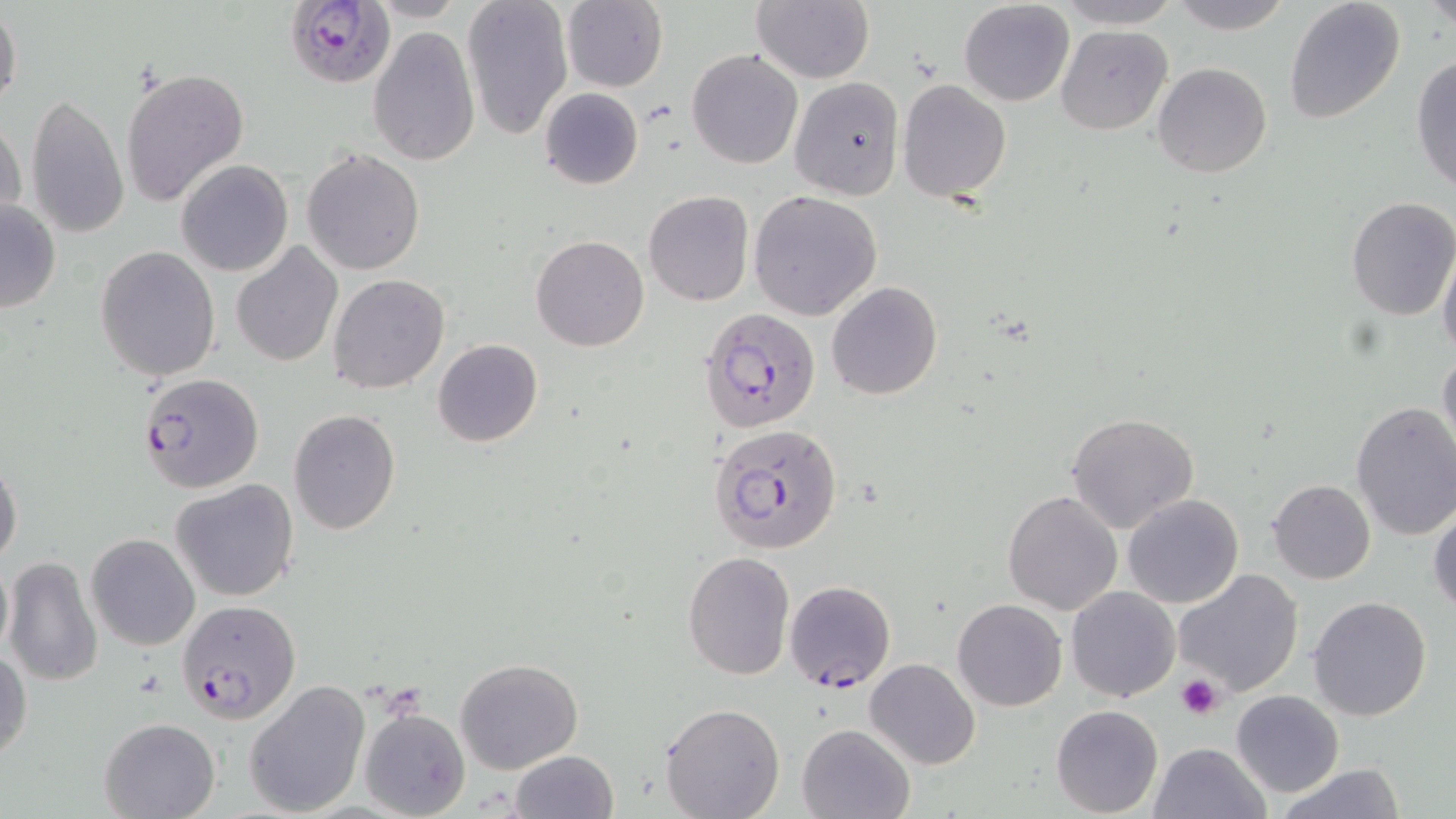
Approximate bounding boxes as (x1, y1, x2, y2) in pixels. Uninfected red blood cell locations: (462, 0, 573, 141), (561, 0, 668, 92), (751, 0, 874, 84), (1165, 0, 1294, 33), (958, 1, 1074, 106), (1056, 1, 1181, 30), (1283, 1, 1406, 125), (1428, 1, 1453, 34), (0, 5, 23, 115), (1055, 26, 1174, 135), (367, 27, 480, 166), (686, 48, 804, 170), (1411, 53, 1456, 197), (1153, 63, 1272, 179), (121, 66, 249, 208), (789, 76, 905, 201), (897, 81, 1012, 203), (538, 87, 644, 189), (24, 93, 131, 240), (0, 115, 26, 232), (301, 148, 426, 275), (176, 160, 293, 277), (748, 190, 882, 321), (643, 191, 754, 307), (1346, 198, 1456, 320), (0, 199, 61, 313), (532, 235, 649, 351), (229, 242, 342, 367), (1438, 244, 1456, 359), (95, 247, 221, 381), (229, 255, 447, 378), (328, 273, 449, 394), (826, 282, 943, 401), (432, 339, 543, 447), (1437, 346, 1456, 463), (1350, 401, 1456, 542), (287, 409, 401, 534), (1067, 412, 1200, 534), (0, 458, 23, 568), (171, 479, 300, 603), (1267, 480, 1376, 584), (1003, 489, 1124, 614), (1122, 494, 1243, 609), (1429, 501, 1456, 617), (85, 533, 200, 651), (0, 551, 13, 668), (682, 552, 795, 679), (2, 554, 104, 688), (1172, 568, 1305, 698), (1066, 586, 1180, 701), (1308, 596, 1433, 721), (952, 598, 1067, 711), (0, 647, 31, 766), (454, 656, 584, 773), (865, 659, 980, 769), (244, 679, 370, 817), (1231, 689, 1344, 796), (659, 702, 785, 819), (1050, 704, 1163, 817), (359, 707, 471, 819), (99, 717, 219, 819), (796, 723, 914, 819), (1148, 742, 1270, 819), (510, 750, 618, 819), (1272, 764, 1408, 819). Platelet locations: (1176, 675, 1225, 720). Plasmodium falciparum-infected red blood cell locations: (286, 0, 394, 87), (699, 305, 823, 432), (137, 373, 264, 493), (713, 423, 842, 556), (784, 579, 896, 692), (178, 601, 301, 724). Slide-level diagnosis: Plasmodium falciparum. One field of a larger specimen. Thin blood film. 1000x magnification. May-Grünwald-Giemsa-stained preparation. Light microscopy. Image is 1456×819 pixels.